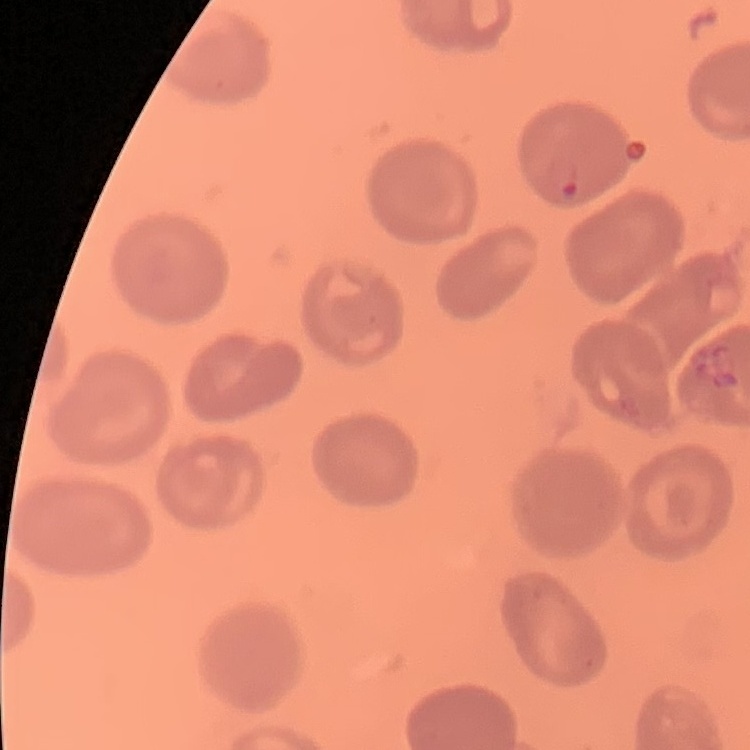

The red blood cells show no rouleaux formation. Field's or Giemsa stain. Thin blood film. Square crop of a larger photomicrograph.